Give the extent of all Trypanosoma brucei.
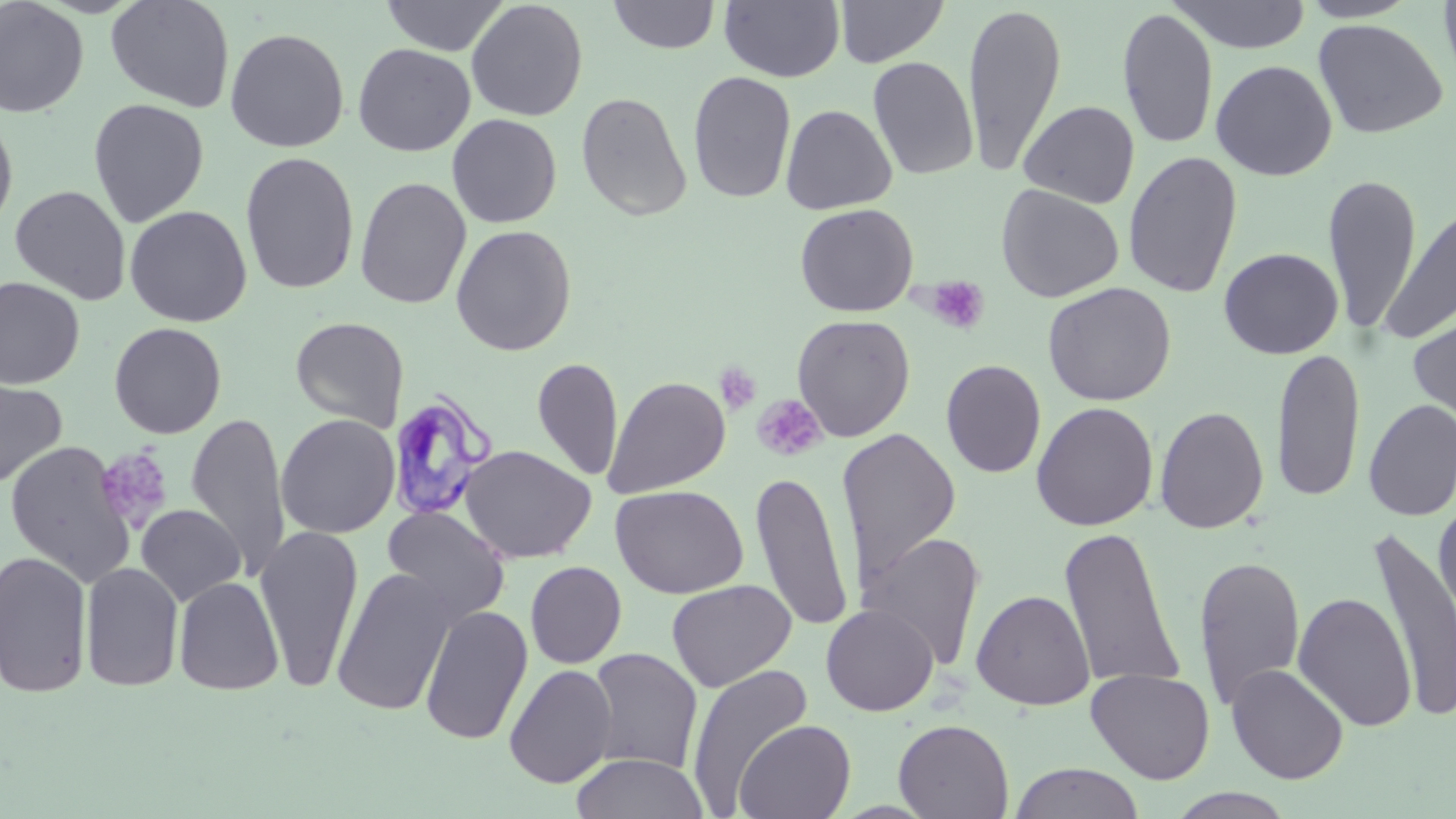

Approximate bounding boxes as (x1, y1, x2, y2) in pixels.
Trypanosoma brucei: (387, 392, 500, 522).

slide_level_diagnosis: Trypanosoma brucei
image_size: 1456×819 pixels
magnification: 1000x
stain: May-Grünwald-Giemsa
field_of_view: one of a larger specimen
preparation: thin blood smear
uninfected_red_blood_cell_locations: 'approximate bounding boxes as (x1, y1, x2, y2) in pixels: (105, 0, 235, 113), (380, 0, 509, 56), (465, 0, 588, 122), (607, 0, 722, 54), (720, 0, 845, 83), (835, 0, 949, 67), (1168, 0, 1312, 53), (1298, 0, 1419, 22), (1438, 0, 1456, 89), (0, 1, 89, 118), (962, 3, 1067, 177), (1117, 7, 1219, 150), (1312, 18, 1449, 139), (224, 27, 350, 153), (352, 43, 475, 157), (867, 56, 979, 180), (1211, 59, 1337, 181), (687, 71, 797, 204), (575, 91, 693, 221), (88, 98, 210, 227), (1019, 100, 1139, 208), (780, 104, 897, 215), (0, 111, 19, 236), (446, 114, 562, 229), (1123, 150, 1243, 298), (240, 151, 360, 295), (1322, 172, 1422, 335), (355, 176, 471, 309), (996, 183, 1124, 302), (9, 185, 131, 304), (1381, 201, 1455, 345), (795, 203, 918, 317), (124, 205, 253, 327), (451, 224, 577, 356), (1218, 247, 1344, 359), (0, 276, 85, 390), (1042, 281, 1177, 406), (1407, 303, 1456, 436), (791, 314, 915, 441), (290, 316, 409, 432), (109, 322, 227, 438), (1271, 345, 1366, 504), (532, 356, 623, 482), (941, 359, 1047, 479), (604, 375, 731, 498), (0, 376, 68, 489), (1362, 399, 1456, 521), (1031, 401, 1159, 531), (1155, 405, 1269, 534), (187, 412, 290, 580), (276, 414, 399, 538), (837, 428, 961, 586), (4, 441, 136, 586), (459, 445, 596, 563), (751, 469, 853, 633), (610, 485, 748, 598), (1434, 497, 1456, 643), (136, 504, 246, 605), (382, 506, 510, 625), (254, 526, 364, 692), (1059, 526, 1186, 692), (1370, 527, 1456, 723), (862, 531, 987, 670), (0, 549, 93, 698), (1193, 554, 1306, 712), (525, 561, 627, 668), (80, 562, 184, 692), (331, 567, 458, 716), (174, 575, 285, 696), (666, 579, 796, 692), (971, 589, 1095, 711), (1293, 592, 1417, 731), (820, 603, 939, 716), (420, 605, 534, 745), (586, 648, 703, 775), (1225, 663, 1349, 784), (504, 664, 617, 788), (686, 665, 814, 811), (1086, 668, 1215, 784), (893, 718, 1014, 818), (733, 719, 856, 819), (571, 752, 709, 819), (1009, 762, 1146, 819), (1167, 788, 1298, 818)'
platelet_locations: 'approximate bounding boxes as (x1, y1, x2, y2) in pixels: (922, 275, 990, 335), (713, 362, 762, 415), (752, 394, 827, 462), (94, 445, 173, 532)'
modality: light microscopy